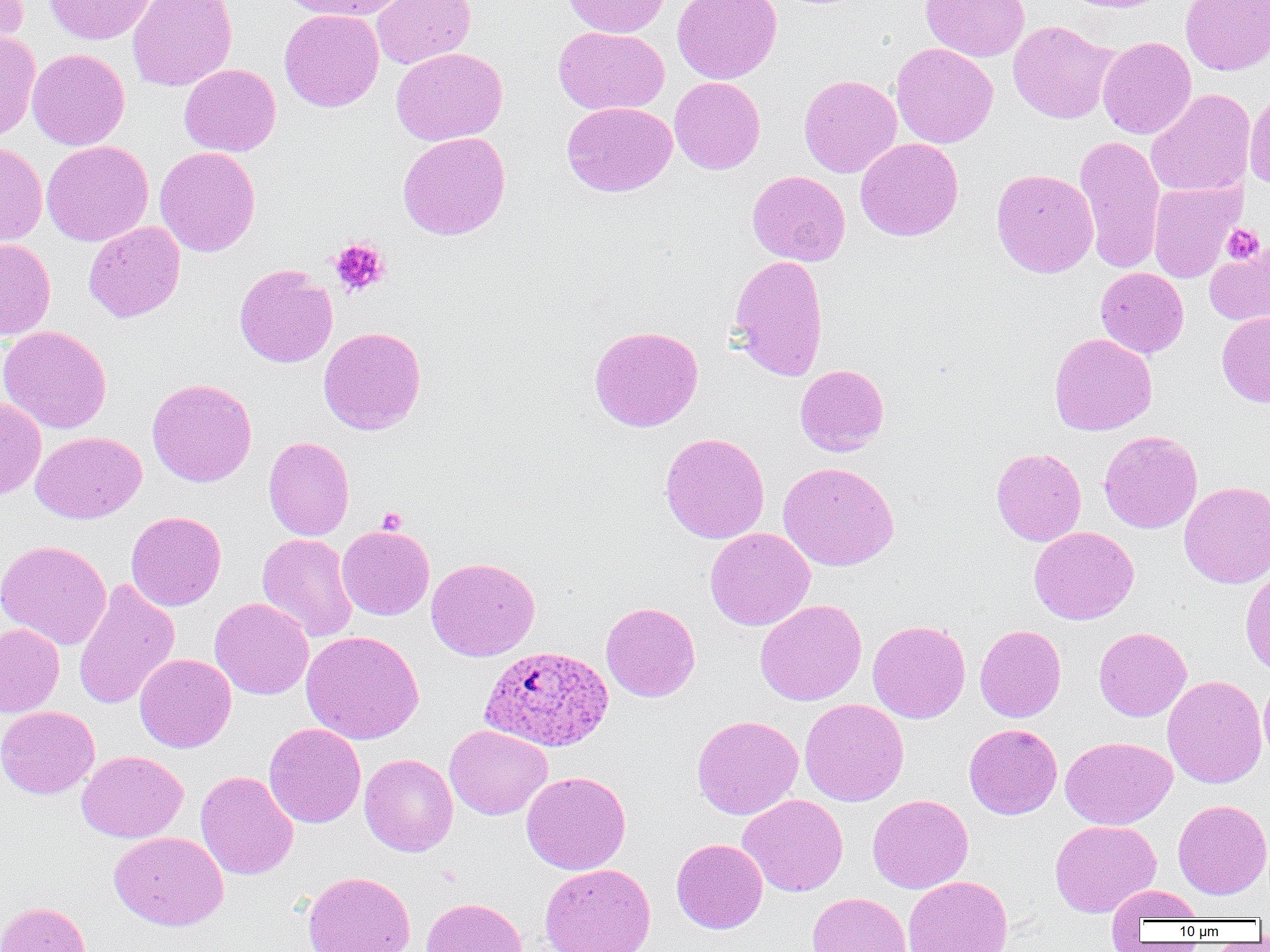
Approximate bounding boxes as (x1, y1, x2, y2) in pixels. Uninfected red blood cell locations: (0, 0, 29, 59), (44, 0, 156, 45), (128, 0, 238, 91), (279, 0, 407, 20), (372, 0, 475, 69), (563, 0, 668, 38), (673, 0, 782, 84), (920, 0, 1030, 62), (1060, 0, 1176, 13), (1180, 0, 1270, 75), (279, 9, 383, 112), (1008, 21, 1117, 124), (553, 26, 669, 115), (0, 30, 41, 142), (1097, 36, 1197, 139), (891, 43, 997, 148), (391, 47, 507, 146), (27, 48, 130, 150), (179, 63, 281, 157), (799, 75, 902, 178), (670, 77, 765, 174), (1146, 88, 1255, 197), (1244, 88, 1270, 191), (562, 102, 676, 196), (397, 131, 511, 240), (1074, 134, 1165, 273), (855, 138, 963, 242), (41, 140, 154, 246), (0, 141, 48, 246), (154, 147, 261, 257), (991, 168, 1099, 278), (747, 170, 850, 266), (1148, 181, 1243, 282), (83, 221, 185, 323), (0, 238, 56, 340), (1204, 244, 1270, 327), (728, 254, 829, 381), (234, 264, 338, 368), (1095, 267, 1189, 358), (1217, 311, 1270, 407), (0, 325, 111, 434), (319, 326, 427, 435), (589, 326, 703, 432), (1049, 333, 1157, 436), (795, 364, 889, 456), (147, 377, 257, 487), (0, 396, 46, 499), (1099, 430, 1202, 534), (31, 431, 146, 523), (660, 432, 770, 544), (263, 436, 354, 540), (991, 447, 1086, 546), (778, 462, 899, 571), (1179, 481, 1270, 588), (126, 511, 226, 611), (336, 524, 434, 620), (1028, 526, 1139, 625), (705, 527, 815, 631), (257, 533, 357, 642), (0, 540, 112, 650), (426, 557, 540, 661), (1240, 564, 1270, 678), (73, 578, 180, 711), (210, 598, 314, 699), (755, 599, 867, 706), (600, 601, 701, 702), (867, 620, 970, 723), (0, 623, 64, 718), (975, 625, 1066, 722), (1094, 627, 1191, 722), (301, 630, 424, 745), (134, 653, 236, 753), (1162, 674, 1266, 789), (1259, 674, 1270, 768), (799, 698, 909, 806), (0, 706, 100, 799), (692, 714, 803, 820), (264, 723, 366, 828), (964, 723, 1062, 819), (444, 724, 552, 820), (1060, 736, 1177, 830), (76, 750, 188, 842), (359, 753, 458, 856), (195, 771, 298, 880), (521, 771, 631, 875), (738, 794, 848, 897), (867, 794, 973, 893), (1172, 799, 1270, 899), (1050, 819, 1161, 917), (109, 831, 229, 931), (671, 838, 768, 933), (539, 863, 656, 952), (302, 871, 416, 952), (902, 876, 1013, 952), (1107, 884, 1205, 927), (807, 892, 912, 952), (421, 897, 528, 952), (0, 901, 90, 952). Platelet locations: (1221, 223, 1265, 265), (329, 237, 391, 297), (377, 507, 407, 534). Plasmodium ovale-infected red blood cell locations: (479, 645, 614, 752). Slide-level diagnosis: Plasmodium ovale. Thin blood smear. Image is 1270×952 pixels. 1000x magnification. Optical microscopy. Single field of view.